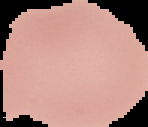
Summary:
  - Image size: 148×127 pixels
  - Result: negative for Plasmodium parasites
  - Image type: segmented cell region with the area outside set to black
  - Preparation: thin blood smear